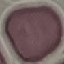

Summary:
  - Result: no malaria parasites detected
  - Capture: smartphone through the microscope eyepiece
  - Stain: Giemsa
  - Image type: cell patch, automatically extracted from a larger field of view and resized to 64 × 64 pixels
  - Preparation: thin blood film